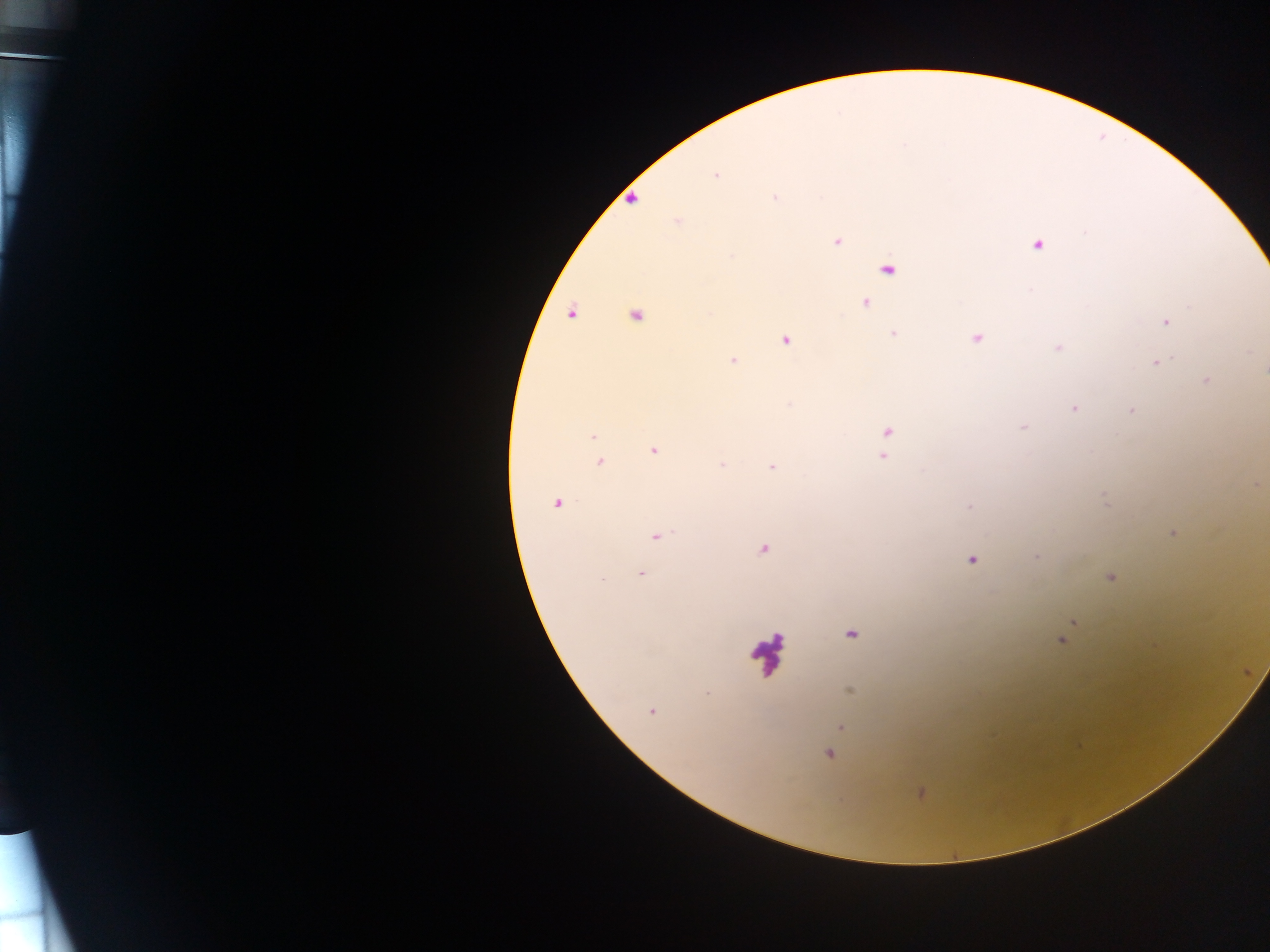

Approximate centers as x y in pixels.
Summary:
  - Malaria parasite locations: 715 175; 775 198; 633 199; 678 222; 837 241; 1037 245; 732 256; 889 270; 866 303; 1190 307; 636 315; 1165 322; 894 334; 976 338; 785 341; 1058 348; 732 360; 1156 362; 1207 381; 1074 408; 1131 410; 1023 427; 888 435; 593 436; 653 451; 885 453; 600 461; 722 466; 772 467; 1256 485; 556 504; 969 507; 1172 534; 657 536; 763 549; 1036 557; 971 560; 640 575; 1110 577; 1074 622; 851 635; 1062 639; 707 692; 651 712; 841 727; 828 754; 921 794
  - Leukocyte locations: 765 651
  - Field of view: single
  - Country: Ghana
  - Image size: 1270×952 pixels
  - Capture: mobile-phone photograph through a microscope
  - Preparation: thick blood smear